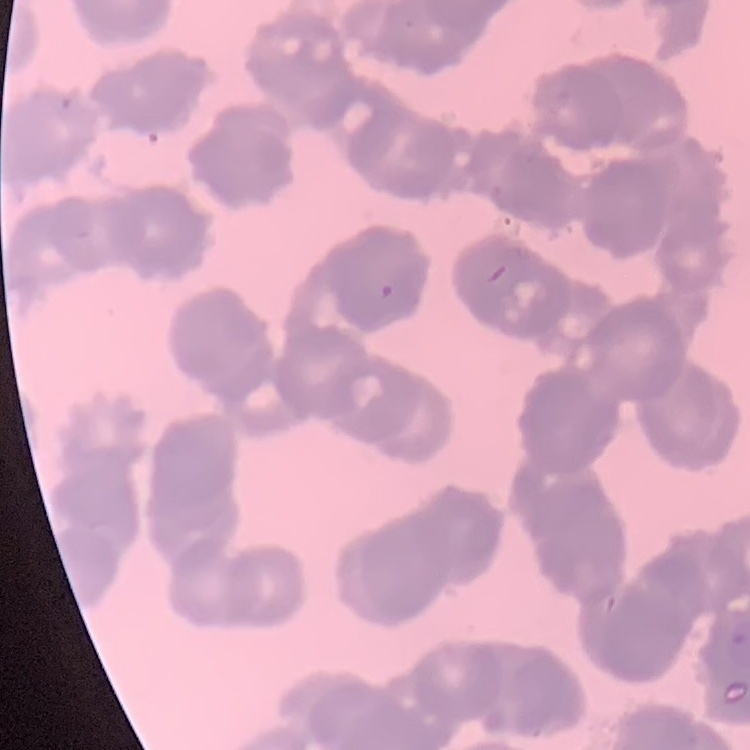
erythrocyte morphology = rouleaux formation
preparation = thin peripheral smear
stain = Field's or Giemsa
image type = one tile cut from a larger photomicrograph